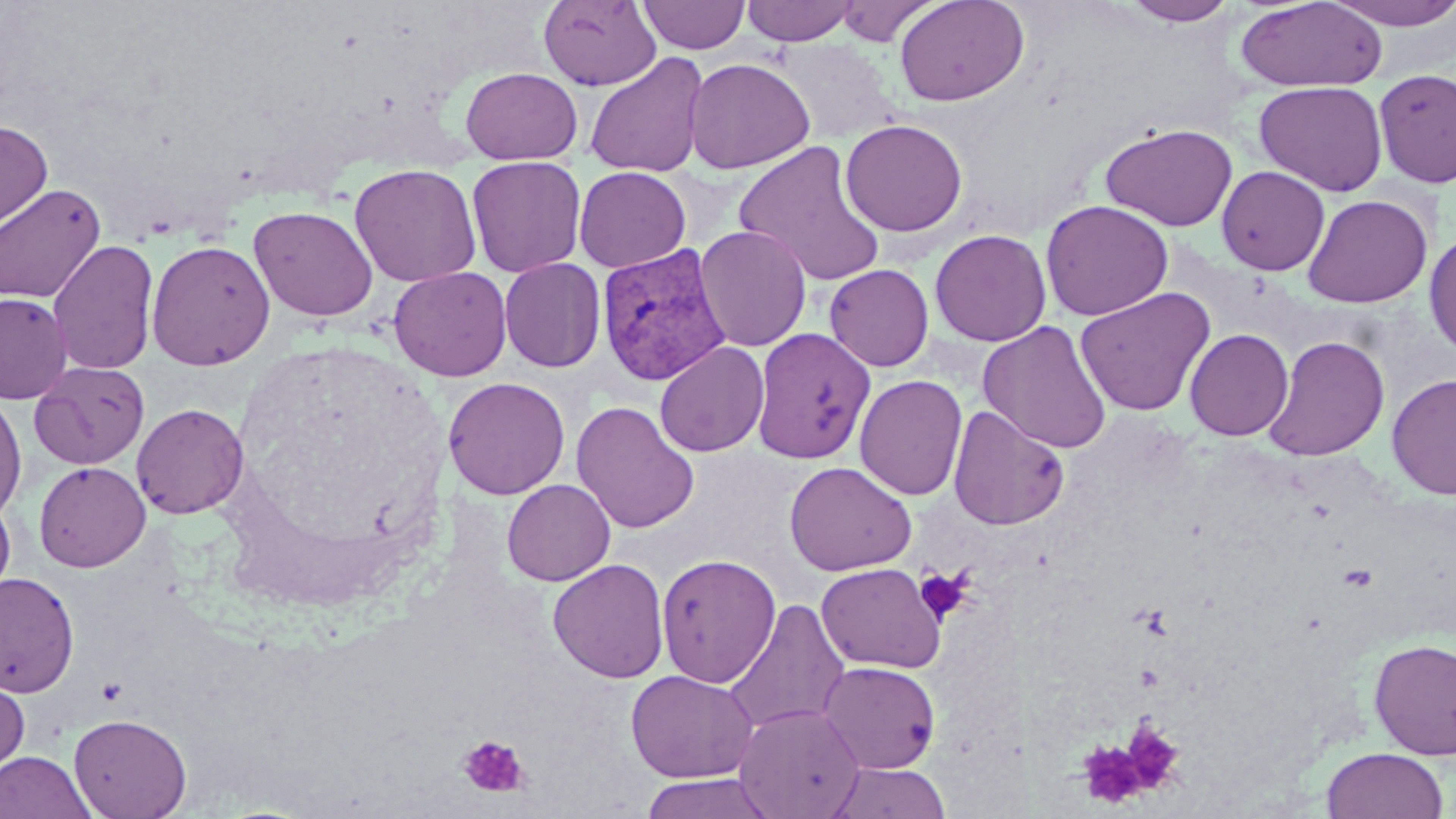
Plasmodium vivax-infected red blood cell locations = approximate bounding boxes as [x1, y1, x2, y2] in pixels: [597, 242, 732, 386]
slide-level diagnosis = Plasmodium vivax
field of view = one of a larger specimen
stain = May-Grünwald-Giemsa
magnification = 1000x
platelet locations = approximate bounding boxes as [x1, y1, x2, y2] in pixels: [915, 567, 974, 624], [1122, 721, 1186, 792], [458, 735, 529, 798], [1076, 741, 1150, 808]
modality = optical microscopy
preparation = thin blood film
image size = 1456×819 pixels
uninfected red blood cell locations = approximate bounding boxes as [x1, y1, x2, y2] in pixels: [538, 0, 662, 91], [638, 0, 750, 54], [741, 0, 859, 45], [894, 0, 1029, 107], [1121, 0, 1239, 26], [1323, 0, 1456, 30], [834, 1, 942, 46], [1235, 1, 1388, 91], [769, 39, 900, 144], [585, 53, 709, 178], [684, 57, 815, 175], [460, 67, 582, 164], [1374, 68, 1456, 188], [1254, 80, 1388, 196], [840, 118, 968, 237], [0, 120, 53, 234], [1100, 122, 1238, 231], [733, 141, 887, 287], [466, 155, 586, 278], [349, 164, 482, 287], [574, 166, 691, 272], [1216, 166, 1330, 275], [0, 183, 106, 304], [1302, 194, 1432, 308], [1039, 199, 1174, 321], [248, 205, 378, 321], [694, 224, 812, 352], [929, 228, 1051, 347], [1424, 230, 1456, 360], [47, 239, 159, 375], [146, 239, 276, 370], [499, 258, 606, 373], [824, 264, 934, 371], [388, 266, 512, 382], [1075, 287, 1215, 416], [0, 292, 73, 403], [978, 321, 1112, 454], [753, 328, 875, 464], [1184, 328, 1294, 441], [1263, 335, 1390, 461], [654, 341, 769, 457], [28, 360, 150, 469], [1387, 373, 1456, 500], [854, 374, 967, 501], [443, 377, 570, 499], [0, 393, 27, 523], [571, 401, 700, 534], [131, 403, 249, 519], [948, 405, 1070, 530], [34, 461, 151, 572], [784, 461, 917, 576], [501, 479, 615, 586], [0, 494, 15, 604], [656, 553, 781, 688], [548, 559, 669, 683], [816, 562, 946, 673], [0, 572, 79, 696], [722, 598, 850, 737], [1369, 638, 1456, 760], [818, 660, 941, 773], [625, 669, 759, 783], [0, 670, 30, 783], [733, 703, 866, 818], [68, 712, 192, 819], [1321, 747, 1449, 819], [0, 750, 96, 819], [826, 761, 951, 819], [637, 772, 780, 819]